State which parasite is depicted.
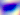

This is Toxoplasma gondii.

Photomicrograph. 400x magnification.